Identify the cell.
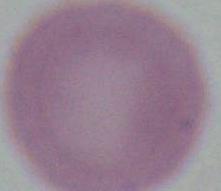
This is an erythrocyte.

Photomicrograph. Captured at 1000x magnification.